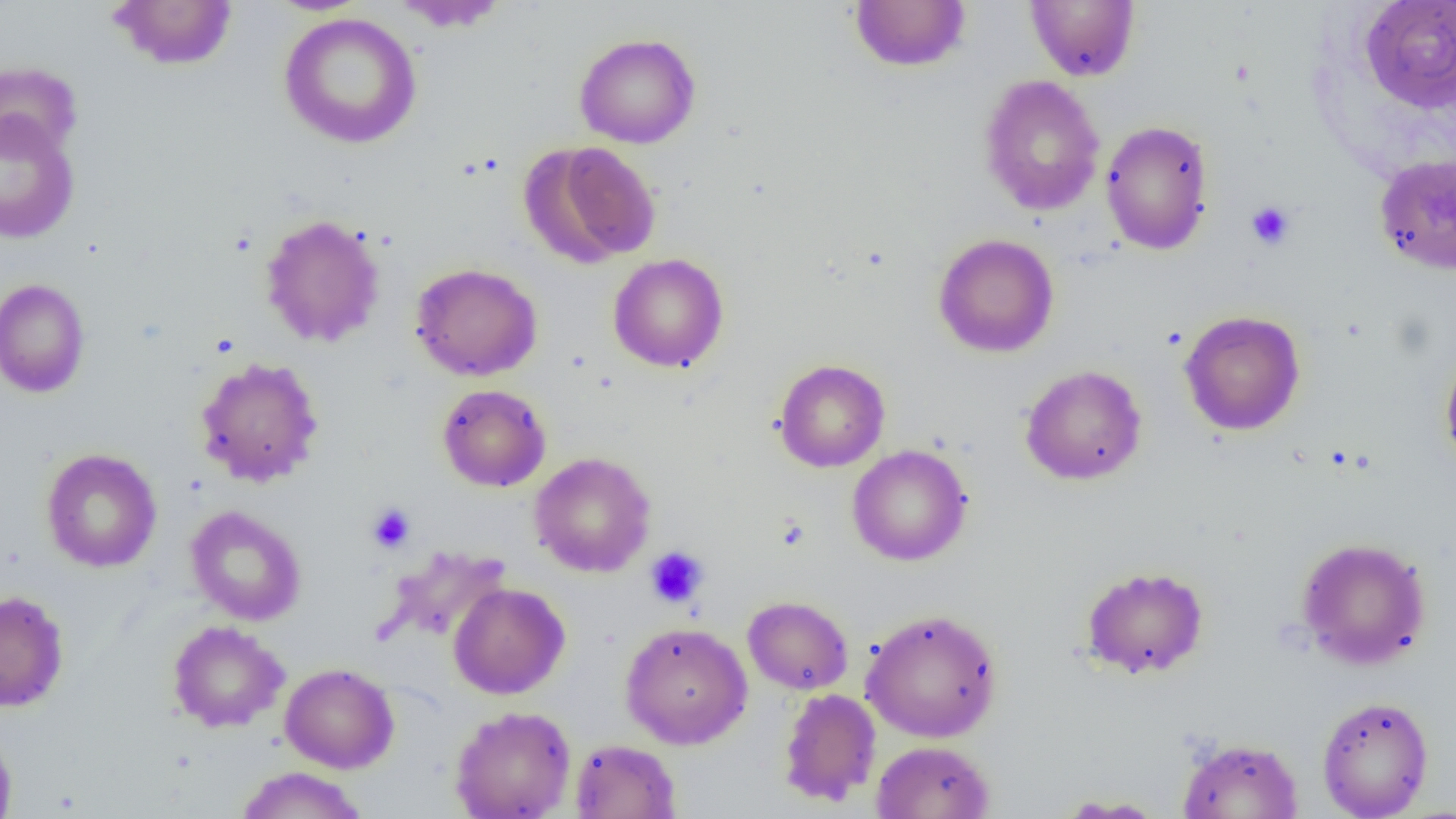 Approximate bounding boxes as (x1,y1)-(x2,y2) corner pairs in pixels. Platelet locations: (1246,201)-(1295,250), (367,503)-(415,553), (645,546)-(708,608). Uninfected red blood cell locations: (109,0)-(237,71), (849,0)-(971,72), (1359,0)-(1456,113), (391,1)-(510,34), (1025,1)-(1139,81), (278,12)-(423,149), (574,32)-(701,149), (0,62)-(82,161), (978,74)-(1106,216), (0,110)-(80,244), (1100,119)-(1214,255), (523,141)-(662,267), (1374,152)-(1456,275), (259,213)-(385,348), (933,233)-(1060,358), (608,253)-(729,373), (410,262)-(543,381), (0,278)-(90,399), (1179,310)-(1306,436), (1439,347)-(1456,472), (194,356)-(324,488), (774,359)-(890,472), (1020,364)-(1147,485), (437,384)-(551,492), (847,445)-(972,566), (41,448)-(162,572), (529,452)-(656,577), (186,505)-(306,626), (1295,536)-(1432,670), (380,545)-(511,647), (1080,565)-(1209,680), (448,582)-(570,699), (1,590)-(69,712), (743,596)-(853,695), (861,608)-(1003,743), (167,620)-(289,733), (620,622)-(753,749), (280,663)-(399,773), (778,688)-(881,807), (1316,695)-(1434,818), (450,706)-(576,819), (0,724)-(17,819), (1177,736)-(1304,818), (569,738)-(681,818), (871,740)-(995,819), (235,766)-(368,819), (1053,795)-(1169,817). Slide-level diagnosis: negative for blood parasites. Optical microscopy. 1000x magnification. Thin blood film. Image is 1456×819 pixels. Single field of view.